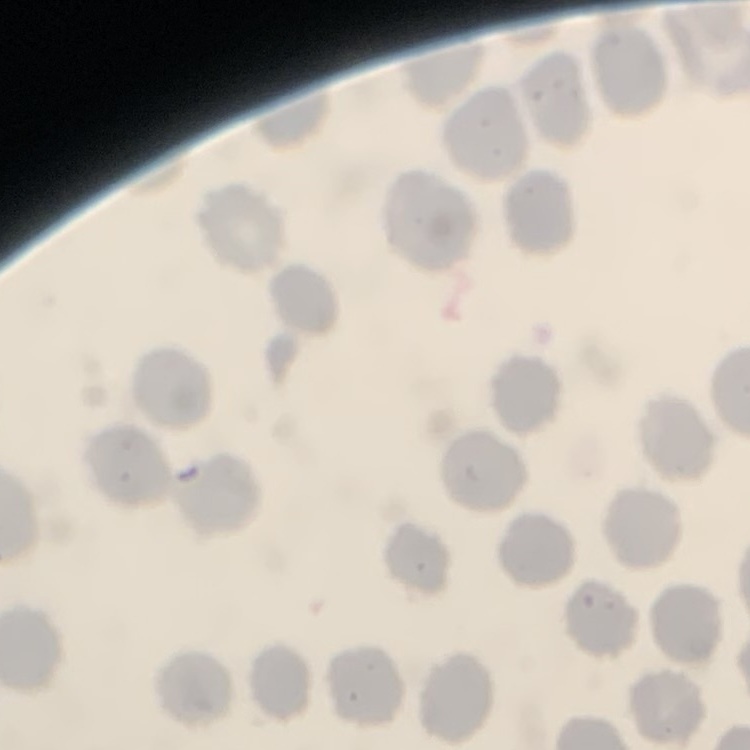

Summary:
  - Red blood cell morphology: no rouleaux formation
  - Stain: Field's or Giemsa
  - Image type: square crop of a larger photomicrograph
  - Preparation: thin blood smear